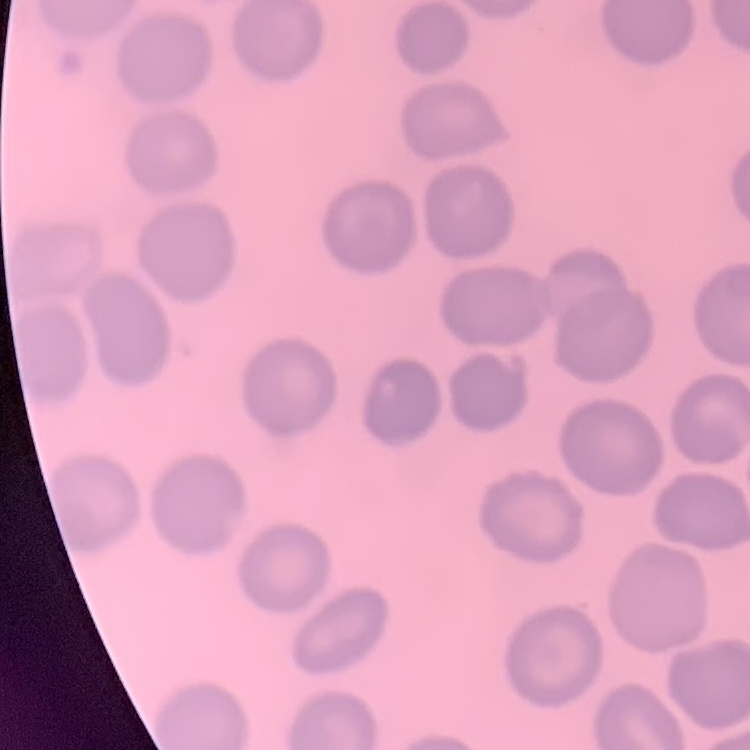

The erythrocytes exhibit no rouleaux formation. Stained with either Field's or Giemsa. Square crop of a larger photomicrograph. Thin peripheral smear.